Locate and identify every blood parasite.
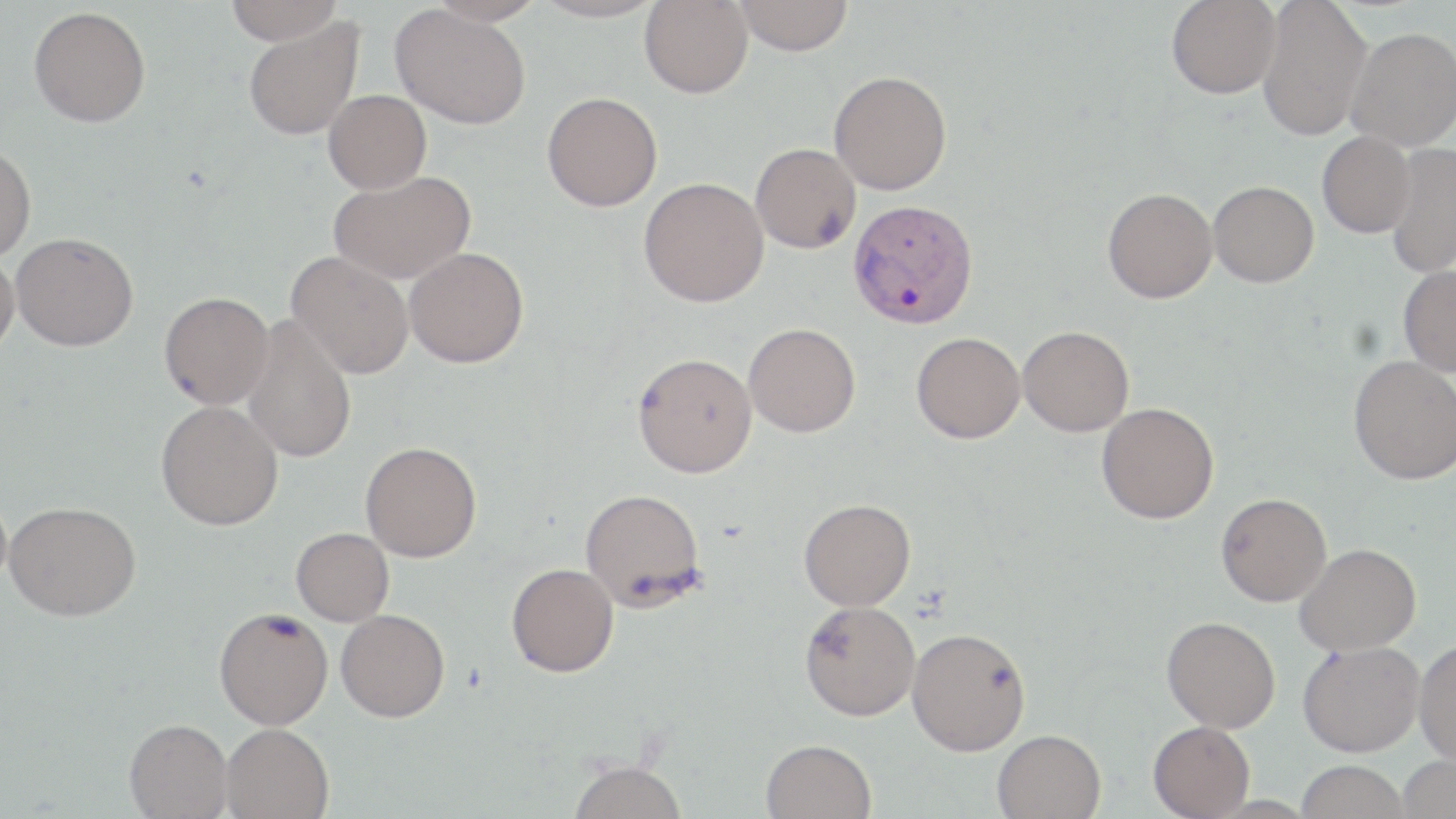

Approximate bounding boxes as (x1, y1, x2, y2) in pixels.
Plasmodium vivax-infected red blood cells: (847, 199, 978, 328).
No Plasmodium falciparum, Plasmodium ovale, Plasmodium malariae, Babesia divergens, or Trypanosoma brucei observed.

slide_level_diagnosis: Plasmodium vivax
modality: optical microscopy
image_size: 1456×819 pixels
field_of_view: one of a larger specimen
preparation: thin blood smear
uninfected_red_blood_cell_locations: 'approximate bounding boxes as (x1, y1, x2, y2) in pixels: (224, 0, 344, 44), (427, 0, 544, 27), (532, 0, 665, 23), (640, 0, 753, 98), (735, 0, 854, 55), (1167, 0, 1280, 98), (1257, 0, 1372, 142), (28, 6, 151, 127), (391, 6, 531, 129), (242, 18, 364, 141), (1345, 27, 1456, 151), (829, 70, 952, 195), (323, 90, 431, 194), (542, 91, 663, 211), (1317, 132, 1415, 238), (0, 142, 36, 262), (750, 142, 861, 253), (1385, 143, 1456, 279), (328, 170, 476, 284), (638, 177, 769, 307), (1208, 180, 1318, 287), (1102, 188, 1217, 303), (10, 232, 138, 351), (404, 247, 529, 368), (286, 251, 415, 379), (0, 252, 19, 358), (1397, 265, 1456, 377), (158, 292, 273, 410), (242, 315, 358, 464), (743, 323, 860, 437), (1018, 325, 1134, 436), (911, 332, 1026, 443), (632, 352, 758, 478), (1348, 355, 1456, 485), (156, 400, 283, 530), (1097, 402, 1219, 524), (360, 441, 482, 562), (579, 488, 706, 610), (1216, 493, 1331, 606), (798, 498, 916, 610), (4, 500, 141, 621), (291, 527, 394, 625), (1295, 543, 1421, 655), (506, 563, 618, 677), (800, 600, 921, 720), (214, 606, 333, 730), (336, 609, 449, 722), (1162, 616, 1280, 732), (907, 627, 1031, 755), (1414, 639, 1456, 766), (1297, 640, 1425, 757), (125, 718, 233, 818), (1148, 720, 1255, 818), (221, 722, 334, 819), (992, 729, 1106, 819), (761, 738, 877, 819), (1397, 754, 1456, 819), (566, 759, 688, 819), (1295, 760, 1409, 818)'
stain: May-Grünwald-Giemsa
magnification: 1000x